Name the blood parasite species.
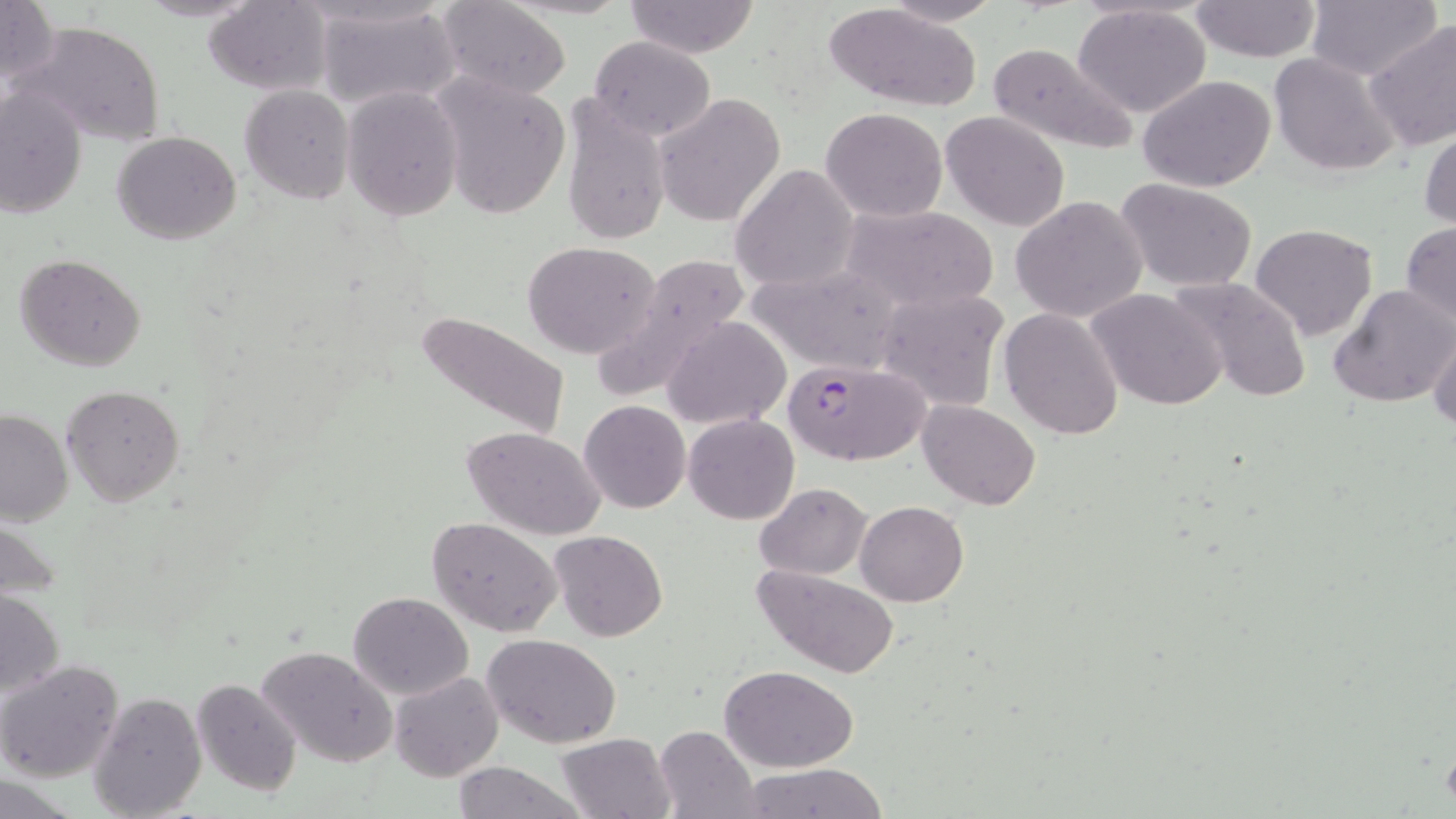

Plasmodium falciparum.

Approximate bounding boxes as named x1/y1/x2/y2 corners in pixels. Uninfected red blood cell locations: (x1=134, y1=0, x2=261, y2=22), (x1=882, y1=0, x2=1005, y2=25), (x1=1190, y1=0, x2=1321, y2=61), (x1=1304, y1=0, x2=1441, y2=81), (x1=0, y1=1, x2=58, y2=87), (x1=204, y1=1, x2=332, y2=95), (x1=435, y1=1, x2=572, y2=100), (x1=624, y1=1, x2=761, y2=57), (x1=824, y1=3, x2=985, y2=113), (x1=314, y1=4, x2=461, y2=112), (x1=1072, y1=4, x2=1211, y2=116), (x1=1362, y1=20, x2=1455, y2=154), (x1=15, y1=21, x2=166, y2=148), (x1=588, y1=35, x2=716, y2=142), (x1=986, y1=40, x2=1139, y2=157), (x1=1268, y1=52, x2=1399, y2=176), (x1=431, y1=73, x2=571, y2=221), (x1=1138, y1=74, x2=1277, y2=191), (x1=240, y1=85, x2=355, y2=203), (x1=0, y1=86, x2=88, y2=222), (x1=341, y1=86, x2=465, y2=222), (x1=558, y1=93, x2=672, y2=248), (x1=652, y1=94, x2=785, y2=227), (x1=820, y1=108, x2=947, y2=222), (x1=941, y1=111, x2=1070, y2=231), (x1=1419, y1=120, x2=1455, y2=234), (x1=112, y1=130, x2=242, y2=244), (x1=730, y1=164, x2=859, y2=293), (x1=1117, y1=179, x2=1258, y2=292), (x1=1011, y1=196, x2=1148, y2=323), (x1=841, y1=204, x2=997, y2=311), (x1=1400, y1=220, x2=1456, y2=327), (x1=1249, y1=222, x2=1378, y2=342), (x1=522, y1=240, x2=663, y2=358), (x1=15, y1=252, x2=147, y2=372), (x1=596, y1=254, x2=754, y2=398), (x1=747, y1=264, x2=904, y2=375), (x1=1168, y1=274, x2=1314, y2=404), (x1=1327, y1=284, x2=1456, y2=408), (x1=873, y1=287, x2=1009, y2=411), (x1=1087, y1=287, x2=1226, y2=411), (x1=999, y1=307, x2=1124, y2=442), (x1=413, y1=309, x2=572, y2=440), (x1=662, y1=316, x2=794, y2=429), (x1=1428, y1=324, x2=1456, y2=434), (x1=61, y1=385, x2=185, y2=505), (x1=578, y1=400, x2=690, y2=513), (x1=918, y1=400, x2=1039, y2=511), (x1=0, y1=408, x2=73, y2=525), (x1=684, y1=413, x2=799, y2=525), (x1=460, y1=425, x2=608, y2=540), (x1=753, y1=484, x2=873, y2=578), (x1=856, y1=500, x2=969, y2=605), (x1=1, y1=516, x2=66, y2=599), (x1=426, y1=516, x2=561, y2=634), (x1=550, y1=529, x2=667, y2=641), (x1=753, y1=564, x2=901, y2=679), (x1=1, y1=588, x2=65, y2=701), (x1=347, y1=591, x2=474, y2=699), (x1=484, y1=635, x2=622, y2=749), (x1=258, y1=645, x2=399, y2=768), (x1=0, y1=660, x2=125, y2=784), (x1=720, y1=664, x2=859, y2=772), (x1=389, y1=670, x2=504, y2=782), (x1=191, y1=677, x2=303, y2=799), (x1=87, y1=690, x2=208, y2=819), (x1=653, y1=725, x2=760, y2=818), (x1=555, y1=733, x2=674, y2=819), (x1=453, y1=761, x2=584, y2=819), (x1=740, y1=765, x2=888, y2=819). Plasmodium falciparum-infected red blood cell locations: (x1=786, y1=359, x2=932, y2=466). One field of a larger specimen. Captured at 1000x magnification. Light microscopy. Image is 1456×819 pixels. Thin blood smear. May-Grünwald-Giemsa-stained preparation.